State which parasite is depicted.
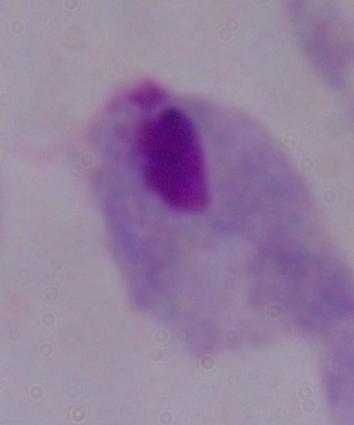
A trichomonad.

modality = photomicrograph
magnification = 1000x